Assess this cell for malaria.
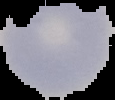
Uninfected.

Summary:
  - Image type: segmented cell region with the area outside set to black
  - Image size: 115×100 pixels
  - Preparation: thin blood film